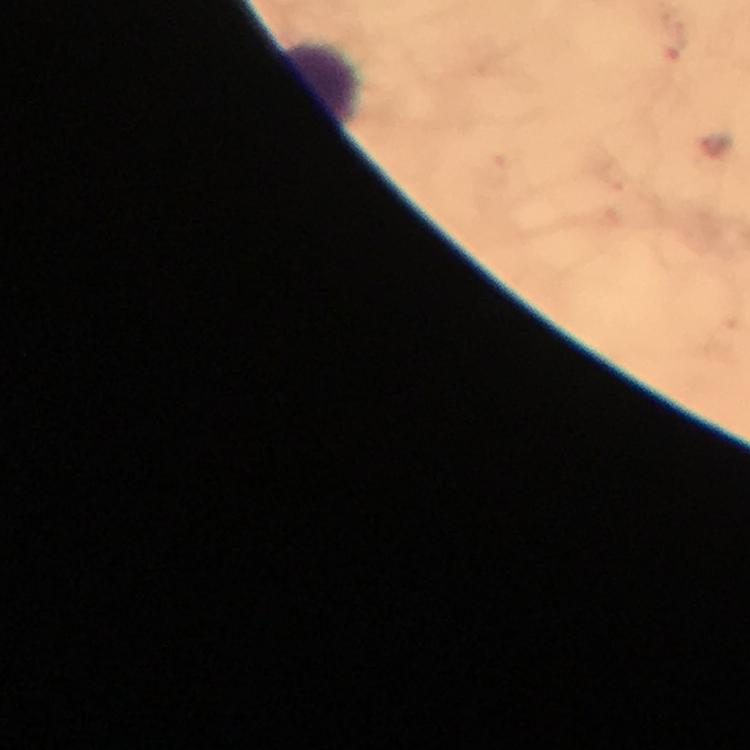

Approximate object centers, in pixels from the top-left corner.
Summary:
  - Leukocyte locations: (x=319, y=85)
  - Image size: 750×750 pixels
  - Preparation: thick blood smear
  - Immersion oil: used
  - Context: from a diagnostic examination for malaria
  - Plasmodium parasites: none detected
  - Capture: smartphone camera through the microscope
  - Stain: Giemsa
  - Cropped from: one field of view
  - Magnification: 100x